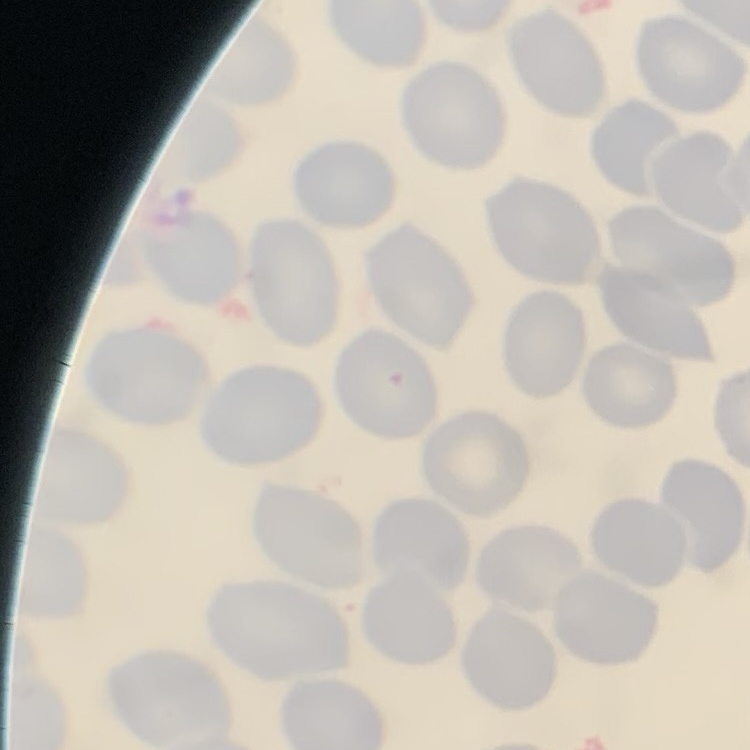
Summary:
  - Erythrocyte morphology: no rouleaux formation
  - Preparation: thin blood film
  - Image type: square crop of a larger photomicrograph
  - Stain: Field's or Giemsa